Identify the blood parasite species.
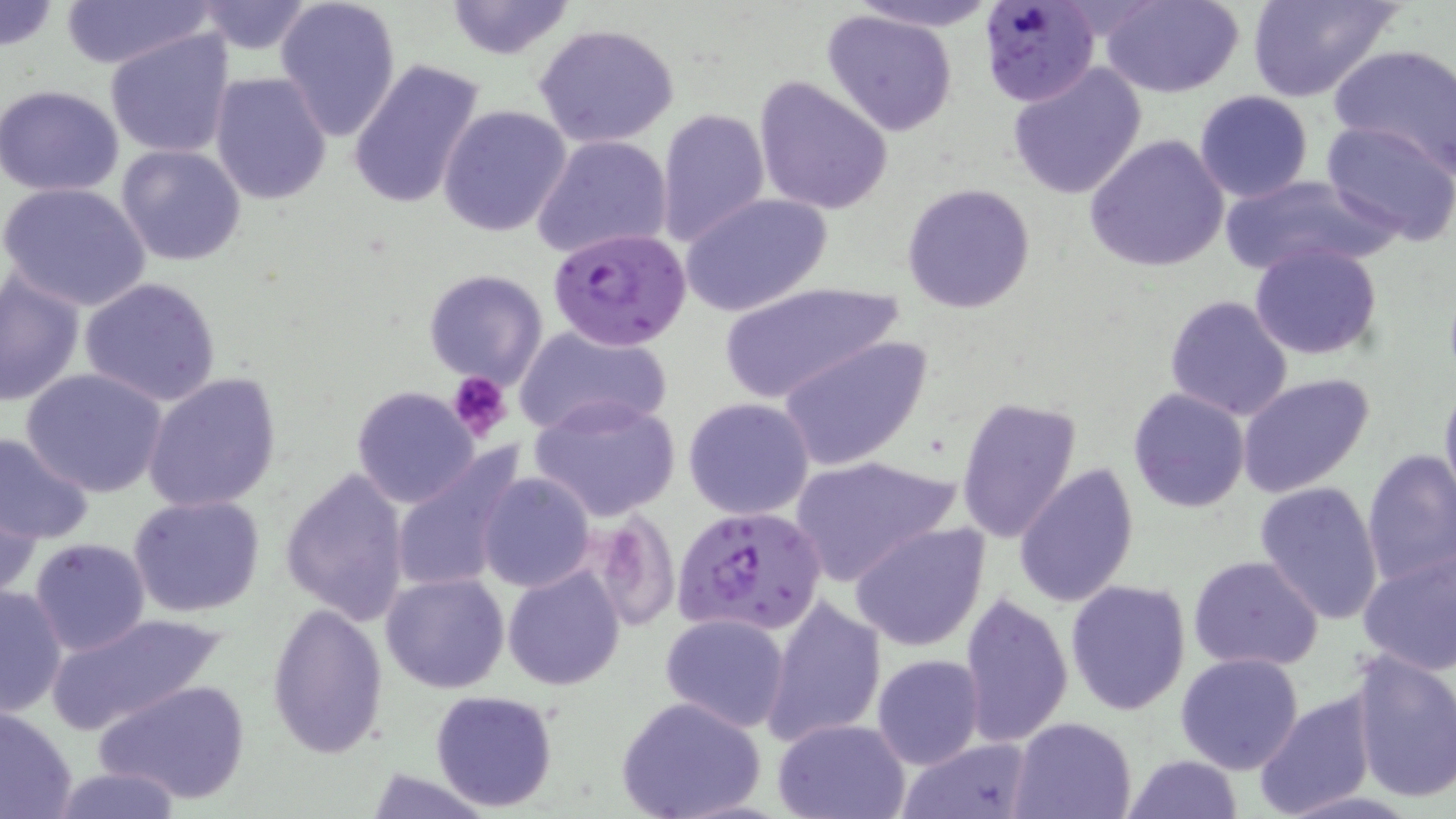

Plasmodium falciparum.

Summary:
  - Coordinate format: approximate bounding boxes as (x1,y1)-(x2,y2) corner pairs in pixels
  - Platelet locations: (446,370)-(511,443)
  - Plasmodium falciparum-infected red blood cell locations: (977,1)-(1102,107), (549,226)-(691,351), (673,504)-(827,637)
  - Uninfected red blood cell locations: (0,0)-(58,52), (54,0)-(219,69), (274,0)-(402,142), (843,0)-(1006,33), (1100,0)-(1247,98), (1250,0)-(1402,104), (193,1)-(318,54), (443,1)-(576,59), (822,9)-(960,136), (533,23)-(682,149), (106,31)-(234,158), (1328,42)-(1456,174), (347,57)-(486,212), (1006,62)-(1148,200), (211,72)-(333,205), (755,75)-(893,215), (0,85)-(127,198), (1193,91)-(1314,205), (438,105)-(571,237), (658,108)-(769,248), (1321,119)-(1456,246), (1084,133)-(1231,273), (531,134)-(673,261), (116,144)-(247,266), (1218,173)-(1393,279), (1,182)-(152,311), (901,182)-(1036,314), (680,192)-(833,318), (1249,242)-(1383,361), (422,269)-(549,389), (0,271)-(85,408), (77,276)-(225,408), (715,283)-(904,404), (1164,295)-(1295,422), (514,324)-(670,439), (777,335)-(933,471), (20,368)-(169,499), (141,372)-(282,512), (1237,375)-(1374,499), (1438,376)-(1456,512), (351,386)-(480,508), (1127,387)-(1250,514), (529,395)-(682,523), (954,396)-(1083,547), (683,397)-(816,520), (0,431)-(95,546), (390,445)-(528,597), (1361,449)-(1456,591), (788,455)-(961,585), (1015,465)-(1138,610), (279,466)-(411,627), (477,473)-(593,593), (1255,480)-(1385,624), (0,489)-(39,601), (127,493)-(266,618), (851,523)-(989,652), (29,538)-(151,656), (1357,548)-(1456,675), (1188,556)-(1325,672), (502,564)-(625,691), (380,572)-(511,694), (1065,578)-(1193,715), (0,584)-(69,718), (957,593)-(1071,748), (763,597)-(886,747), (267,600)-(391,761), (44,611)-(229,737), (660,613)-(790,732), (1348,651)-(1456,805), (873,653)-(987,770), (1175,653)-(1304,774), (94,677)-(252,806), (1252,688)-(1377,817), (430,689)-(559,812), (616,696)-(766,819), (0,705)-(77,819), (1012,716)-(1136,819), (771,717)-(913,819), (898,737)-(1033,819), (1124,753)-(1243,819), (42,765)-(188,819), (360,768)-(492,818)
  - Magnification: 1000x
  - Preparation: thin blood smear
  - Image size: 1456×819 pixels
  - Field of view: single
  - Stain: May-Grünwald-Giemsa
  - Modality: light microscopy